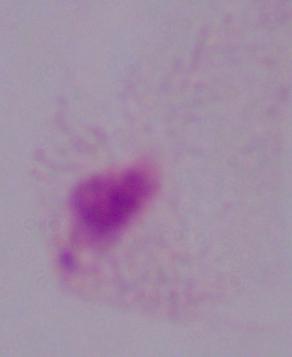
identification = trichomonad
magnification = 1000x
modality = photomicrograph